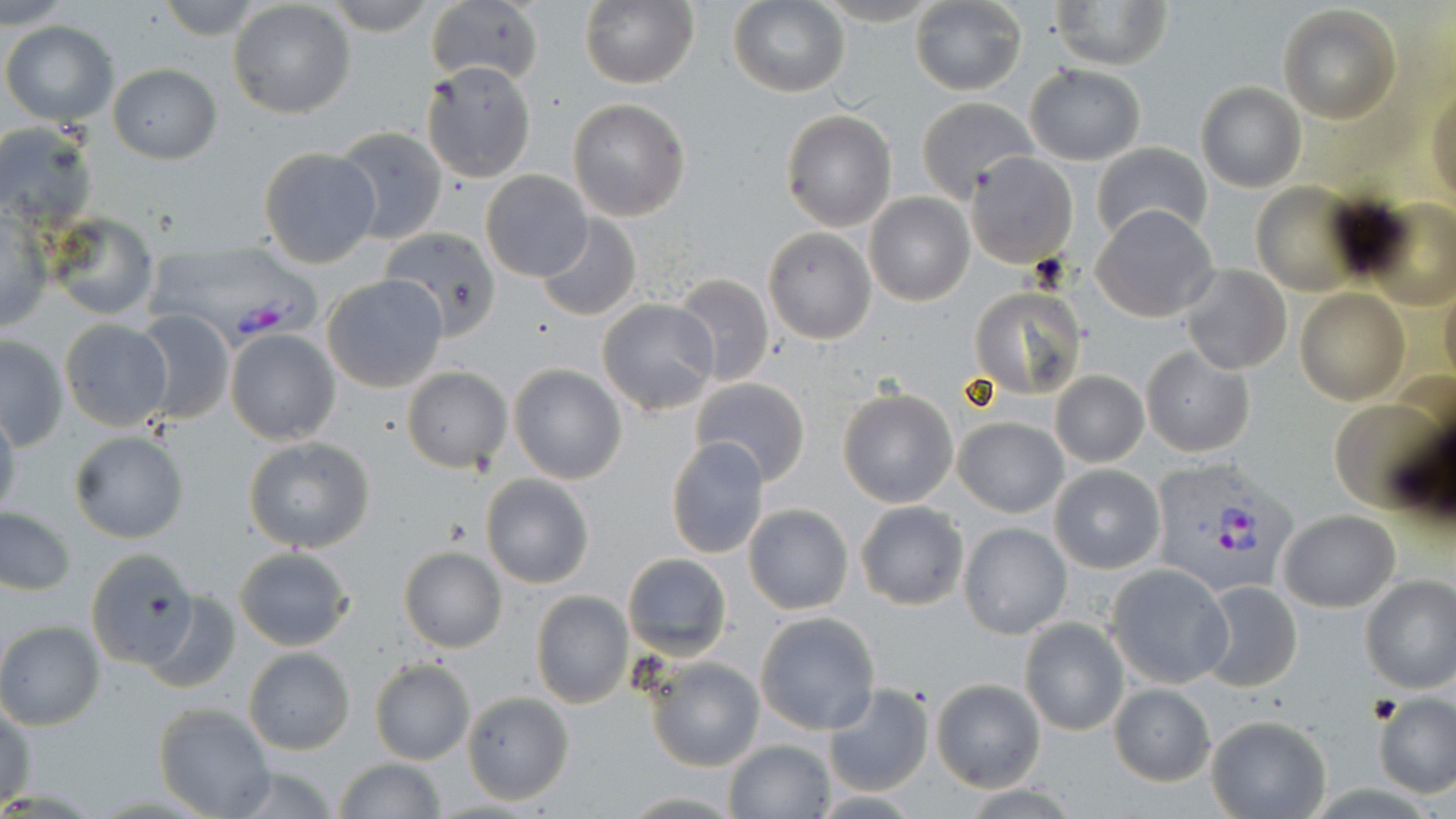

Summary:
  - Coordinate format: approximate bounding boxes as (x1, y1, x2, y2) in pixels
  - Plasmodium vivax-infected red blood cell locations: (144, 244, 324, 352), (1145, 458, 1299, 598)
  - Uninfected red blood cell locations: (155, 0, 267, 38), (321, 0, 441, 36), (424, 0, 543, 88), (1049, 0, 1173, 70), (0, 1, 78, 31), (228, 1, 356, 118), (580, 1, 698, 88), (908, 1, 1026, 94), (727, 2, 850, 97), (1277, 5, 1401, 124), (1, 20, 118, 126), (422, 61, 536, 183), (108, 64, 221, 164), (1025, 64, 1146, 163), (1195, 82, 1304, 192), (1429, 87, 1455, 207), (915, 96, 1037, 203), (567, 98, 691, 221), (780, 109, 898, 231), (1, 122, 98, 226), (333, 128, 449, 245), (1091, 142, 1213, 244), (258, 146, 380, 267), (965, 152, 1079, 268), (480, 170, 593, 282), (1251, 183, 1363, 294), (864, 194, 974, 306), (1365, 199, 1456, 308), (1091, 204, 1219, 323), (0, 212, 53, 332), (43, 214, 160, 321), (535, 214, 641, 322), (379, 228, 502, 342), (763, 228, 876, 344), (1180, 265, 1291, 376), (672, 273, 775, 387), (321, 274, 448, 393), (1440, 278, 1456, 395), (968, 286, 1087, 399), (1296, 289, 1407, 405), (596, 298, 721, 416), (135, 311, 235, 424), (59, 321, 174, 431), (226, 328, 340, 445), (1, 336, 69, 449), (1141, 346, 1254, 458), (509, 363, 626, 484), (402, 366, 512, 473), (1051, 370, 1147, 467), (691, 377, 811, 487), (837, 388, 960, 509), (1331, 391, 1453, 515), (0, 405, 20, 521), (955, 417, 1067, 517), (69, 429, 190, 543), (244, 436, 377, 553), (665, 436, 770, 557), (1049, 464, 1164, 573), (480, 473, 595, 588), (855, 501, 969, 610), (743, 503, 854, 615), (0, 508, 76, 595), (1278, 510, 1400, 611), (958, 523, 1071, 639), (236, 545, 354, 652), (398, 545, 508, 653), (80, 546, 198, 670), (622, 553, 732, 659), (1106, 564, 1231, 688), (1359, 575, 1456, 694), (1195, 580, 1302, 692), (530, 591, 633, 708), (141, 592, 241, 695), (755, 611, 882, 735), (1019, 618, 1129, 737), (0, 621, 105, 730), (243, 648, 355, 754), (643, 654, 764, 772), (369, 659, 476, 765), (931, 678, 1045, 791), (823, 682, 934, 797), (1108, 684, 1216, 785), (461, 691, 575, 805), (1374, 695, 1456, 796), (1, 701, 36, 809), (153, 702, 276, 818), (1205, 715, 1330, 819), (725, 739, 833, 817), (333, 758, 447, 817), (215, 762, 344, 819), (615, 792, 746, 817)
  - Slide-level diagnosis: Plasmodium vivax
  - Image size: 1456×819 pixels
  - Preparation: thin blood smear
  - Field of view: one of a larger specimen
  - Magnification: 1000x
  - Stain: May-Grünwald-Giemsa
  - Modality: optical microscopy